Classify this cell by malaria status.
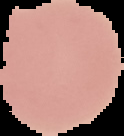
Uninfected.

Cell region segmented out of the field of view; the surrounding area is masked to black. From a thin blood film. Image is 124×136 pixels.